Outline each Plasmodium vivax-infected red blood cell.
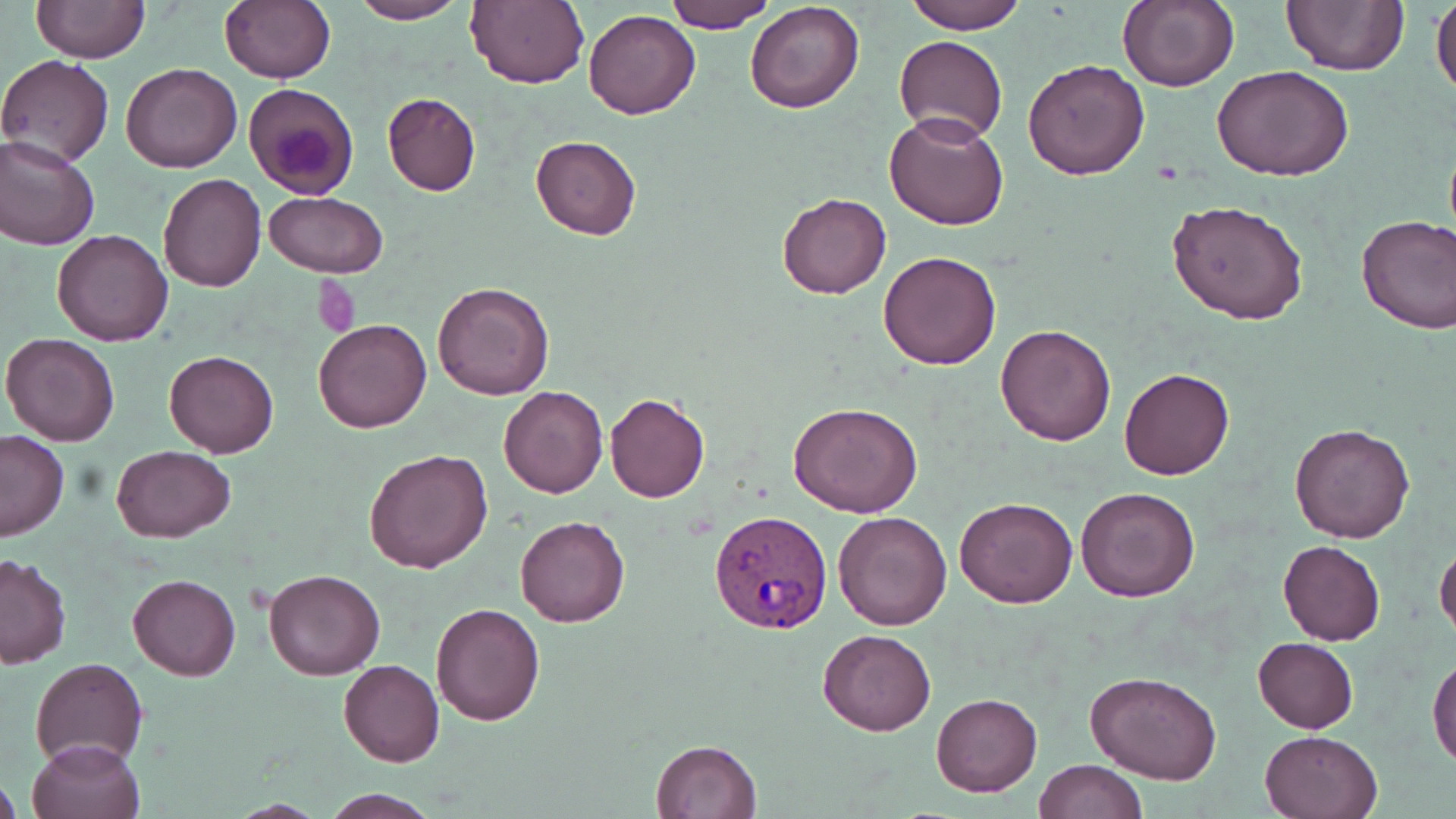
Approximate bounding boxes as (x1,y1)-(x2,y2) corner pairs in pixels.
Plasmodium vivax-infected red blood cells: (709,508)-(833,635).

slide_level_diagnosis: Plasmodium vivax
field_of_view: single
preparation: thin blood film
magnification: 1000x
modality: light microscopy
stain: May-Grünwald-Giemsa
uninfected_red_blood_cell_locations: 'approximate bounding boxes as (x1,y1)-(x2,y2) corner pairs in pixels: (32,0)-(147,62), (220,0)-(335,83), (665,0)-(777,30), (903,0)-(1026,34), (1117,0)-(1239,92), (1431,0)-(1456,101), (347,1)-(467,24), (465,1)-(589,89), (745,2)-(866,114), (1280,2)-(1409,75), (582,9)-(700,121), (895,34)-(1007,146), (0,55)-(114,167), (1022,59)-(1149,181), (122,64)-(242,172), (1212,65)-(1357,183), (243,82)-(359,199), (382,92)-(480,197), (885,112)-(1009,231), (0,134)-(100,250), (531,135)-(642,239), (158,174)-(268,293), (263,191)-(390,277), (776,192)-(892,301), (1166,199)-(1309,326), (1355,213)-(1456,335), (52,230)-(176,346), (878,250)-(1003,370), (433,280)-(554,401), (314,319)-(432,434), (994,322)-(1118,445), (1,332)-(121,446), (164,350)-(279,458), (1118,368)-(1235,480), (498,385)-(609,498), (605,392)-(710,502), (789,402)-(922,518), (1289,423)-(1415,543), (0,432)-(70,541), (110,445)-(236,543), (363,447)-(494,574), (1074,486)-(1201,603), (953,496)-(1077,608), (833,509)-(952,631), (514,513)-(631,628), (1277,540)-(1386,645), (1434,541)-(1456,643), (0,554)-(72,668), (262,567)-(386,680), (128,574)-(240,681), (431,603)-(545,725), (818,628)-(935,737), (1253,637)-(1358,732), (1428,656)-(1456,768), (29,657)-(149,770), (338,660)-(444,766), (1084,672)-(1223,785), (931,692)-(1042,796), (1259,729)-(1383,819), (25,737)-(145,819), (648,739)-(762,819), (1034,760)-(1147,818), (0,770)-(20,818), (318,790)-(443,818)'
image_size: 1456×819 pixels
platelet_locations: 'approximate bounding boxes as (x1,y1)-(x2,y2) corner pairs in pixels: (310,279)-(361,336)'